Report the malaria status of this cell.
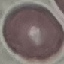
It is uninfected.

Summary:
  - Stain: Giemsa
  - Image type: automatically extracted cell patch, resized to 64 × 64 pixels
  - Preparation: thin blood film
  - Capture: smartphone through the microscope eyepiece